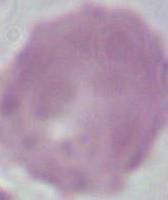
Micrograph. 1000x magnification. An erythrocyte is shown.